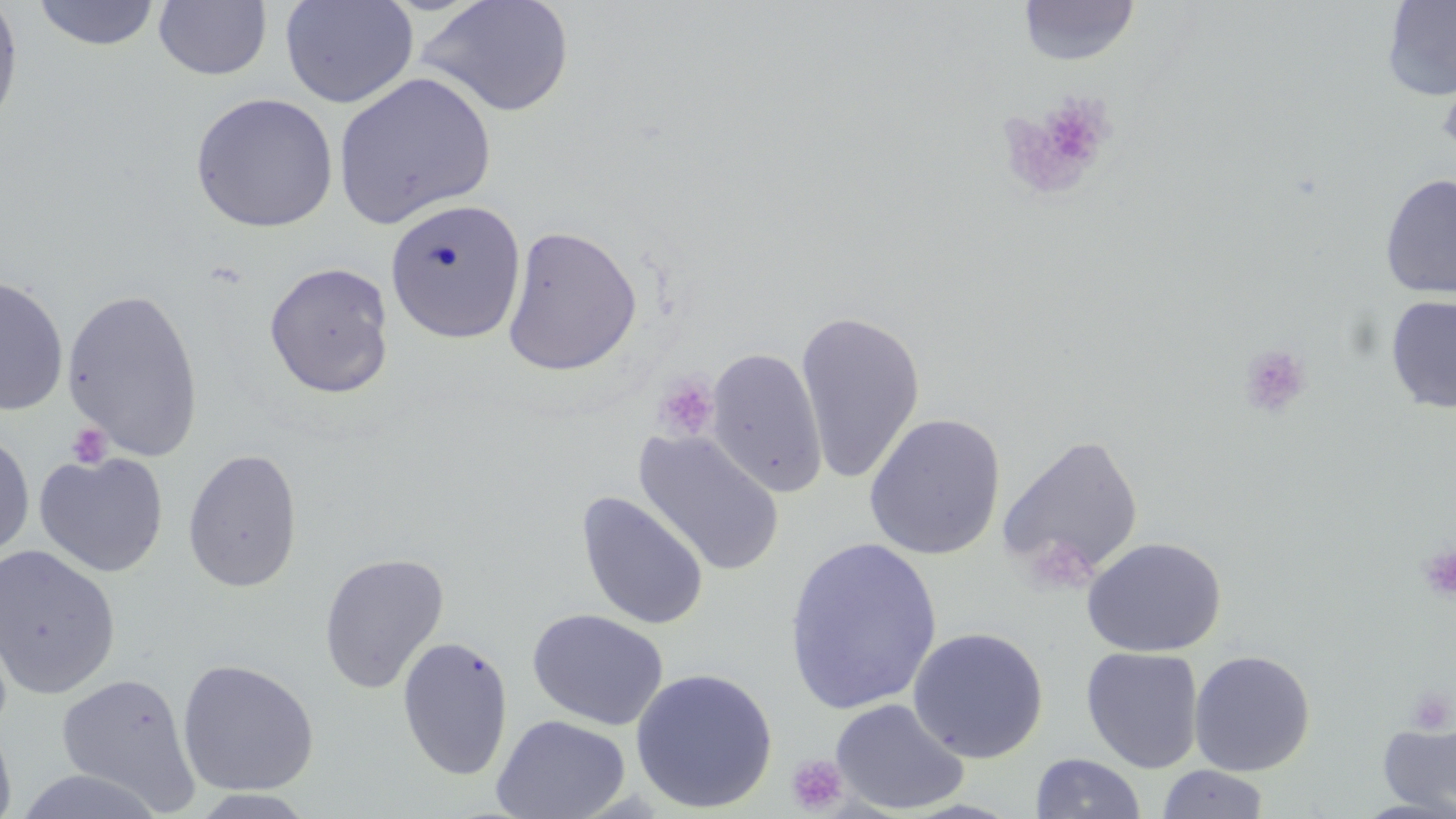 Approximate bounding boxes as named x1/y1/x2/y2 corners in pixels. Uninfected red blood cell locations: (x1=0, y1=0, x2=24, y2=134), (x1=279, y1=0, x2=419, y2=109), (x1=417, y1=0, x2=575, y2=118), (x1=32, y1=1, x2=162, y2=51), (x1=152, y1=1, x2=271, y2=81), (x1=1017, y1=1, x2=1140, y2=67), (x1=1381, y1=1, x2=1456, y2=101), (x1=1437, y1=64, x2=1456, y2=163), (x1=333, y1=71, x2=497, y2=228), (x1=189, y1=91, x2=339, y2=232), (x1=1379, y1=173, x2=1456, y2=299), (x1=385, y1=198, x2=527, y2=344), (x1=502, y1=224, x2=642, y2=376), (x1=263, y1=261, x2=395, y2=399), (x1=0, y1=274, x2=69, y2=416), (x1=62, y1=287, x2=205, y2=459), (x1=1385, y1=295, x2=1456, y2=413), (x1=795, y1=308, x2=925, y2=485), (x1=706, y1=347, x2=828, y2=498), (x1=863, y1=412, x2=1005, y2=560), (x1=633, y1=428, x2=785, y2=577), (x1=1, y1=430, x2=35, y2=561), (x1=997, y1=432, x2=1145, y2=584), (x1=182, y1=448, x2=303, y2=593), (x1=34, y1=452, x2=169, y2=577), (x1=576, y1=491, x2=710, y2=631), (x1=1082, y1=536, x2=1227, y2=657), (x1=783, y1=537, x2=943, y2=716), (x1=0, y1=545, x2=121, y2=700), (x1=318, y1=552, x2=450, y2=693), (x1=528, y1=608, x2=669, y2=730), (x1=908, y1=626, x2=1049, y2=763), (x1=398, y1=636, x2=513, y2=781), (x1=1080, y1=647, x2=1204, y2=773), (x1=1188, y1=649, x2=1316, y2=776), (x1=177, y1=658, x2=320, y2=796), (x1=630, y1=667, x2=778, y2=813), (x1=54, y1=671, x2=202, y2=811), (x1=830, y1=698, x2=970, y2=815), (x1=492, y1=714, x2=631, y2=819), (x1=1378, y1=717, x2=1456, y2=817), (x1=0, y1=719, x2=17, y2=819), (x1=1030, y1=753, x2=1146, y2=818), (x1=1156, y1=765, x2=1271, y2=819), (x1=11, y1=768, x2=169, y2=819), (x1=188, y1=789, x2=317, y2=818). Platelet locations: (x1=1006, y1=97, x2=1115, y2=195), (x1=1239, y1=343, x2=1311, y2=418), (x1=653, y1=375, x2=719, y2=442), (x1=66, y1=422, x2=112, y2=469), (x1=1025, y1=534, x2=1097, y2=594), (x1=1418, y1=546, x2=1456, y2=601), (x1=1406, y1=686, x2=1454, y2=736), (x1=786, y1=754, x2=850, y2=815). Slide-level diagnosis: no evidence of blood parasites. Light microscopy. Captured at 1000x magnification. Image is 1456×819 pixels. Thin blood smear. May-Grünwald-Giemsa-stained preparation. One field of a larger specimen.